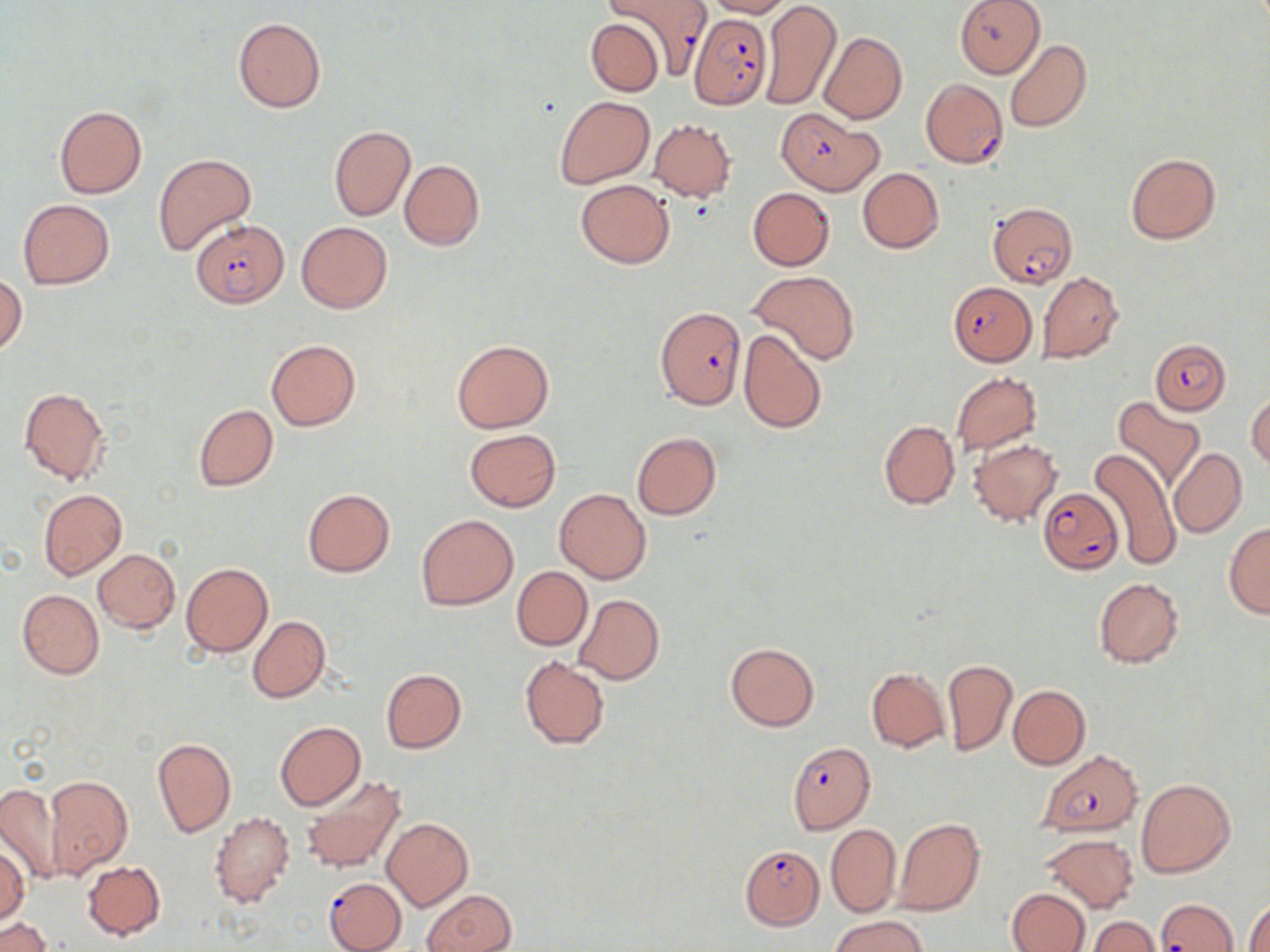

Summary:
  - Coordinate format: approximate bounding boxes as named x1/y1/x2/y2 corners in pixels
  - Uninfected red blood cell locations (subset): (x1=703, y1=0, x2=794, y2=18), (x1=954, y1=0, x2=1045, y2=78), (x1=760, y1=1, x2=840, y2=110), (x1=233, y1=17, x2=327, y2=114), (x1=584, y1=17, x2=665, y2=96), (x1=819, y1=31, x2=907, y2=123), (x1=1005, y1=38, x2=1092, y2=133), (x1=554, y1=95, x2=654, y2=188), (x1=54, y1=106, x2=147, y2=199), (x1=649, y1=120, x2=737, y2=201), (x1=328, y1=125, x2=415, y2=221), (x1=153, y1=153, x2=256, y2=255), (x1=1125, y1=153, x2=1219, y2=244), (x1=400, y1=160, x2=484, y2=249), (x1=858, y1=167, x2=943, y2=253), (x1=575, y1=179, x2=675, y2=268), (x1=748, y1=187, x2=834, y2=271), (x1=18, y1=199, x2=114, y2=289), (x1=296, y1=221, x2=393, y2=313), (x1=747, y1=270, x2=860, y2=364), (x1=1038, y1=271, x2=1124, y2=362), (x1=1, y1=273, x2=27, y2=355), (x1=738, y1=329, x2=827, y2=433), (x1=266, y1=339, x2=360, y2=429), (x1=452, y1=339, x2=553, y2=432), (x1=951, y1=371, x2=1042, y2=454), (x1=19, y1=387, x2=111, y2=486), (x1=1246, y1=390, x2=1270, y2=471), (x1=1112, y1=396, x2=1206, y2=490), (x1=193, y1=404, x2=278, y2=491), (x1=878, y1=420, x2=958, y2=509), (x1=464, y1=429, x2=560, y2=512), (x1=632, y1=433, x2=721, y2=519), (x1=968, y1=439, x2=1063, y2=527), (x1=1088, y1=447, x2=1180, y2=571), (x1=1169, y1=449, x2=1246, y2=537), (x1=553, y1=488, x2=651, y2=583), (x1=39, y1=489, x2=127, y2=581), (x1=302, y1=489, x2=395, y2=577), (x1=416, y1=514, x2=518, y2=610), (x1=1224, y1=522, x2=1270, y2=618), (x1=93, y1=549, x2=180, y2=632), (x1=180, y1=561, x2=273, y2=658), (x1=511, y1=566, x2=592, y2=650), (x1=1094, y1=577, x2=1184, y2=668), (x1=17, y1=589, x2=104, y2=678), (x1=574, y1=594, x2=663, y2=685), (x1=248, y1=615, x2=330, y2=703), (x1=725, y1=642, x2=819, y2=731), (x1=518, y1=656, x2=610, y2=749), (x1=941, y1=657, x2=1018, y2=756), (x1=380, y1=668, x2=467, y2=753), (x1=866, y1=668, x2=950, y2=752), (x1=1008, y1=684, x2=1090, y2=770), (x1=275, y1=721, x2=365, y2=810), (x1=152, y1=737, x2=236, y2=837), (x1=298, y1=775, x2=405, y2=875), (x1=44, y1=776, x2=132, y2=878), (x1=1136, y1=778, x2=1235, y2=878), (x1=0, y1=782, x2=66, y2=884), (x1=210, y1=811, x2=295, y2=908), (x1=383, y1=817, x2=472, y2=910), (x1=892, y1=818, x2=985, y2=916), (x1=825, y1=822, x2=901, y2=917), (x1=1041, y1=833, x2=1138, y2=913), (x1=0, y1=844, x2=29, y2=923), (x1=82, y1=861, x2=166, y2=939), (x1=1005, y1=886, x2=1091, y2=952), (x1=422, y1=889, x2=517, y2=952), (x1=1246, y1=900, x2=1270, y2=952), (x1=830, y1=913, x2=930, y2=952), (x1=1087, y1=916, x2=1159, y2=952), (x1=2, y1=918, x2=50, y2=952)
  - Plasmodium falciparum-infected red blood cell locations (subset): (x1=607, y1=0, x2=711, y2=81), (x1=688, y1=11, x2=772, y2=109), (x1=921, y1=79, x2=1008, y2=168), (x1=776, y1=109, x2=883, y2=196), (x1=987, y1=201, x2=1077, y2=288), (x1=191, y1=219, x2=291, y2=309), (x1=949, y1=281, x2=1037, y2=368), (x1=654, y1=307, x2=746, y2=407), (x1=1152, y1=338, x2=1231, y2=414), (x1=1038, y1=488, x2=1122, y2=573), (x1=1038, y1=750, x2=1144, y2=838), (x1=740, y1=844, x2=825, y2=929), (x1=326, y1=882, x2=407, y2=952), (x1=1156, y1=898, x2=1236, y2=951)
  - Slide-level diagnosis: Plasmodium falciparum
  - Modality: optical microscopy
  - Preparation: thin blood film
  - Magnification: 1000x
  - Stain: May-Grünwald-Giemsa
  - Field of view: single
  - Image size: 1270×952 pixels